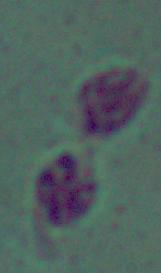
{
  "identification": "Leishmania",
  "modality": "photomicrograph",
  "magnification": "1000x"
}